Locate every Plasmodium ovale-infected red blood cell.
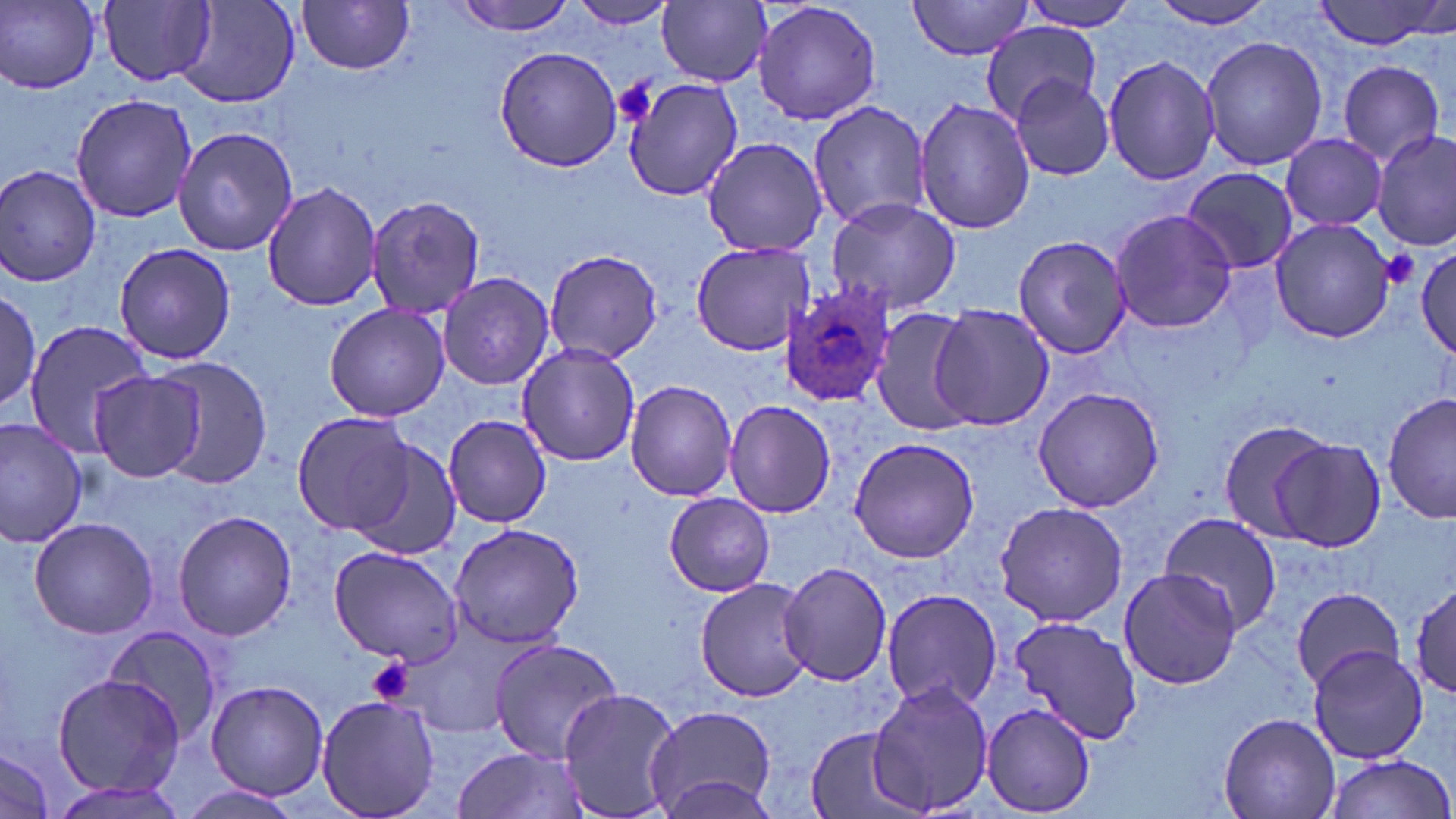

Approximate bounding boxes as (x1,y1)-(x2,y2) corner pairs in pixels.
Plasmodium ovale-infected red blood cells: (778,284)-(895,410).

Uninfected red blood cell locations: (2,0)-(101,92), (456,0)-(580,36), (568,0)-(678,28), (752,0)-(883,126), (908,0)-(1036,60), (1148,0)-(1282,30), (1310,0)-(1453,53), (100,1)-(216,87), (297,1)-(415,75), (1018,1)-(1143,31), (658,2)-(770,87), (182,4)-(301,109), (982,20)-(1101,120), (1199,35)-(1327,172), (492,45)-(624,174), (1102,54)-(1220,187), (1335,58)-(1447,167), (1009,74)-(1118,180), (621,78)-(741,202), (71,94)-(196,222), (916,96)-(1033,236), (807,99)-(930,231), (174,127)-(297,256), (1374,131)-(1453,249), (1280,133)-(1387,230), (701,137)-(831,257), (0,164)-(100,285), (1180,167)-(1298,273), (262,179)-(382,311), (366,194)-(483,320), (825,195)-(962,315), (1111,209)-(1237,332), (1266,217)-(1398,342), (1013,234)-(1133,359), (114,241)-(236,365), (689,241)-(812,355), (1415,246)-(1455,360), (544,250)-(663,363), (437,270)-(554,391), (0,278)-(43,420), (324,302)-(450,421), (931,305)-(1056,429), (871,308)-(982,436), (23,322)-(154,456), (515,342)-(640,465), (146,356)-(274,488), (88,370)-(207,484), (624,378)-(738,500), (1031,385)-(1167,513), (1381,391)-(1455,526), (724,399)-(836,518), (291,410)-(414,536), (442,414)-(552,528), (0,417)-(88,547), (1216,418)-(1333,542), (1269,436)-(1387,553), (848,437)-(981,563), (348,439)-(464,561), (665,493)-(774,597), (994,500)-(1129,629), (173,510)-(297,642), (1159,511)-(1283,634), (28,516)-(157,640), (447,521)-(586,648), (327,546)-(462,664), (777,561)-(892,686), (1117,567)-(1245,689), (697,576)-(812,701), (1411,578)-(1455,702), (1290,586)-(1407,691), (880,588)-(1002,709), (1005,613)-(1142,743), (100,628)-(224,746), (487,637)-(625,762), (1308,645)-(1429,764), (51,672)-(187,798), (203,679)-(330,802), (868,679)-(994,817), (557,688)-(684,819), (315,695)-(441,819), (980,701)-(1099,818), (644,704)-(776,818), (1219,713)-(1341,817), (805,728)-(921,819), (0,746)-(61,819), (453,746)-(588,819), (1323,754)-(1453,819), (46,778)-(193,819), (172,781)-(304,819). Platelet locations: (612,79)-(657,127), (1377,249)-(1420,292), (365,657)-(413,705). Slide-level diagnosis: Plasmodium ovale. One field of a larger specimen. May-Grünwald-Giemsa-stained preparation. Captured at 1000x magnification. Image is 1456×819 pixels. Optical microscopy. Thin blood film.